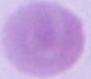
Micrograph. A red blood cell is shown. 1000x magnification.